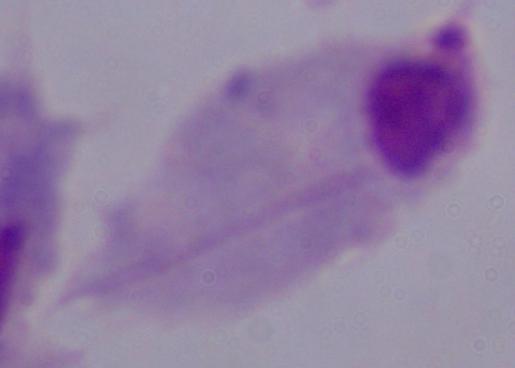
identification: trichomonad
modality: photomicrograph
magnification: 1000x